State which parasite is depicted.
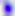

This is Toxoplasma gondii.

modality = photomicrograph
magnification = 400x